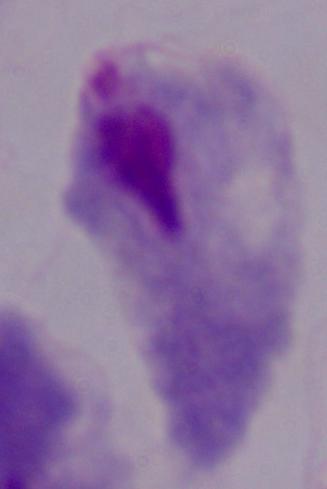

Summary:
  - Identification: trichomonad
  - Magnification: 1000x
  - Modality: micrograph